Classify this cell by malaria status.
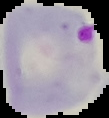

It is parasitized.

Image is 109×118 pixels. From a thin blood smear. Segmented cell region on a black background.